Describe the morphology of the red blood cells.
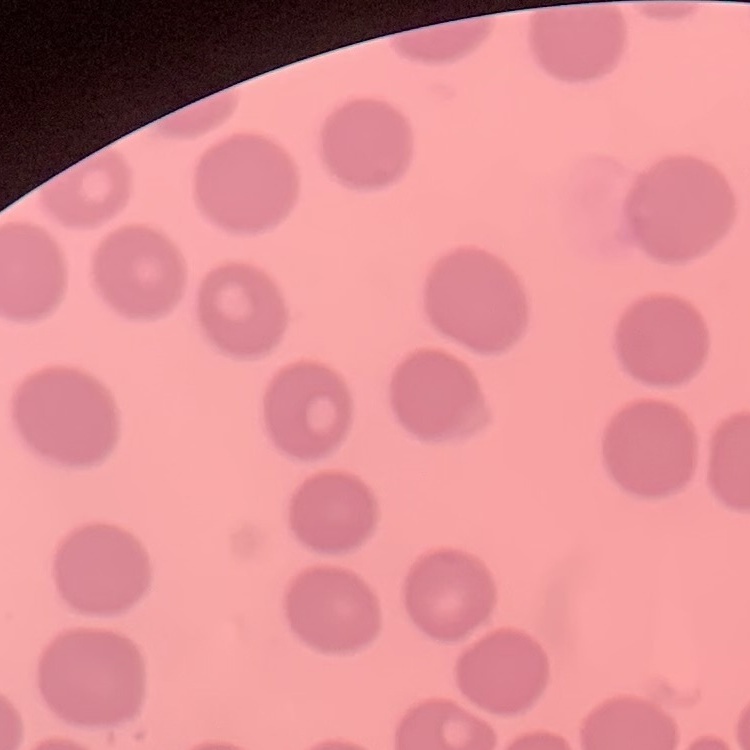
They show no rouleaux formation.

Summary:
  - Stain: Field's or Giemsa
  - Preparation: thin peripheral smear
  - Image type: square crop of a larger photomicrograph